Report the malaria status of this cell.
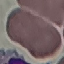
It is uninfected.

Summary:
  - Image type: cell patch, automatically extracted from a larger field of view and resized to 64 × 64 pixels
  - Stain: Giemsa
  - Capture: smartphone through the microscope eyepiece
  - Preparation: thin smear